Give the extent of all Plasmodium falciparum-infected red blood cells.
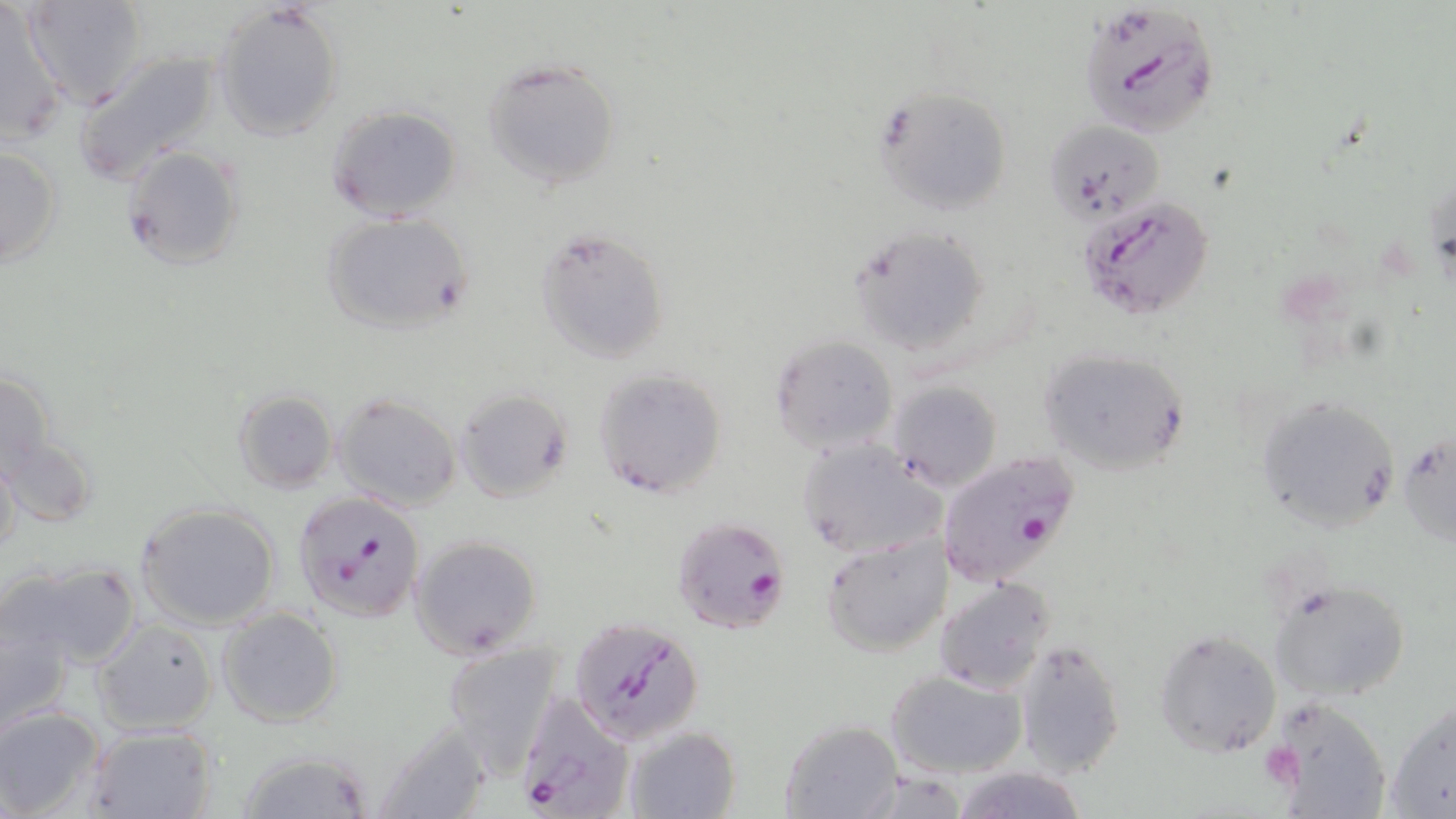
Approximate bounding boxes as named x1/y1/x2/y2 corners in pixels.
Plasmodium falciparum-infected red blood cells: (x1=1078, y1=2, x2=1222, y2=137), (x1=1079, y1=198, x2=1216, y2=322), (x1=937, y1=451, x2=1082, y2=587), (x1=292, y1=492, x2=426, y2=625), (x1=672, y1=514, x2=791, y2=633), (x1=570, y1=616, x2=702, y2=744), (x1=512, y1=690, x2=633, y2=819).

Summary:
  - Uninfected red blood cell locations: (x1=22, y1=0, x2=148, y2=105), (x1=212, y1=3, x2=344, y2=140), (x1=0, y1=5, x2=68, y2=142), (x1=73, y1=46, x2=225, y2=187), (x1=480, y1=56, x2=625, y2=191), (x1=875, y1=88, x2=1012, y2=217), (x1=324, y1=104, x2=462, y2=221), (x1=1044, y1=121, x2=1166, y2=225), (x1=1, y1=143, x2=63, y2=272), (x1=121, y1=144, x2=245, y2=272), (x1=320, y1=212, x2=476, y2=339), (x1=848, y1=225, x2=993, y2=358), (x1=537, y1=228, x2=670, y2=364), (x1=767, y1=335, x2=899, y2=455), (x1=1038, y1=347, x2=1191, y2=477), (x1=1, y1=364, x2=59, y2=486), (x1=592, y1=367, x2=729, y2=500), (x1=887, y1=381, x2=1003, y2=494), (x1=454, y1=388, x2=575, y2=504), (x1=232, y1=391, x2=338, y2=494), (x1=332, y1=391, x2=461, y2=512), (x1=1254, y1=393, x2=1400, y2=531), (x1=1398, y1=430, x2=1456, y2=547), (x1=3, y1=434, x2=96, y2=528), (x1=796, y1=438, x2=943, y2=559), (x1=0, y1=449, x2=21, y2=563), (x1=136, y1=502, x2=282, y2=630), (x1=409, y1=534, x2=542, y2=658), (x1=821, y1=535, x2=953, y2=656), (x1=6, y1=559, x2=141, y2=673), (x1=934, y1=576, x2=1056, y2=693), (x1=1268, y1=576, x2=1411, y2=704), (x1=216, y1=607, x2=343, y2=728), (x1=0, y1=610, x2=75, y2=736), (x1=91, y1=618, x2=217, y2=735), (x1=1155, y1=627, x2=1283, y2=757), (x1=1014, y1=639, x2=1126, y2=777), (x1=441, y1=643, x2=560, y2=774), (x1=885, y1=669, x2=1028, y2=778), (x1=1268, y1=695, x2=1391, y2=816), (x1=1384, y1=698, x2=1456, y2=818), (x1=0, y1=707, x2=105, y2=819), (x1=778, y1=718, x2=904, y2=818), (x1=371, y1=721, x2=492, y2=818), (x1=83, y1=723, x2=219, y2=819), (x1=625, y1=726, x2=741, y2=819), (x1=236, y1=748, x2=374, y2=819), (x1=951, y1=766, x2=1090, y2=819)
  - Platelet locations: (x1=1268, y1=745, x2=1307, y2=783)
  - Slide-level diagnosis: Plasmodium falciparum
  - Preparation: thin blood film
  - Magnification: 1000x
  - Image size: 1456×819 pixels
  - Field of view: one of a larger specimen
  - Stain: May-Grünwald-Giemsa
  - Modality: optical microscopy